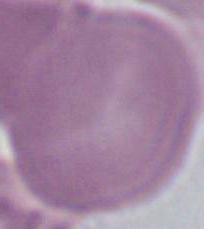

Summary:
  - Identification: erythrocyte
  - Modality: micrograph
  - Magnification: 1000x